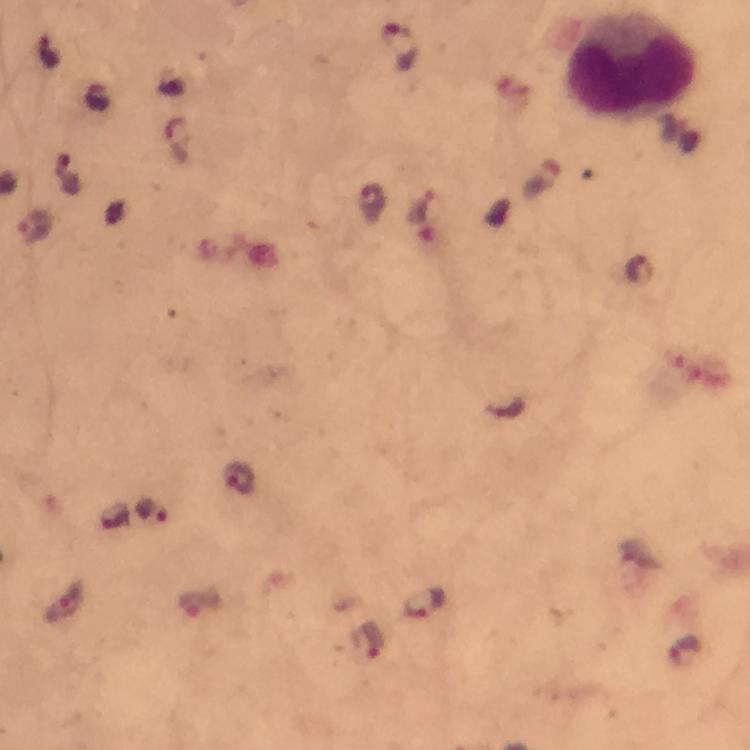
cropped_from: a single field of view
capture: smartphone photograph through a microscope
image_size: 750×750 pixels
preparation: thick blood smear
malaria_parasite_locations: 'approximate object centers, in pixels from the top-left corner: (x=397, y=45), (x=50, y=52), (x=69, y=175), (x=371, y=201), (x=35, y=226), (x=639, y=269), (x=505, y=410), (x=239, y=477), (x=153, y=510), (x=424, y=603), (x=369, y=640), (x=684, y=651)'
magnification: 100x
leukocyte_locations: 'approximate object centers, in pixels from the top-left corner: (x=629, y=69)'
immersion_oil: applied
context: from a malaria diagnostic workup
stain: Giemsa